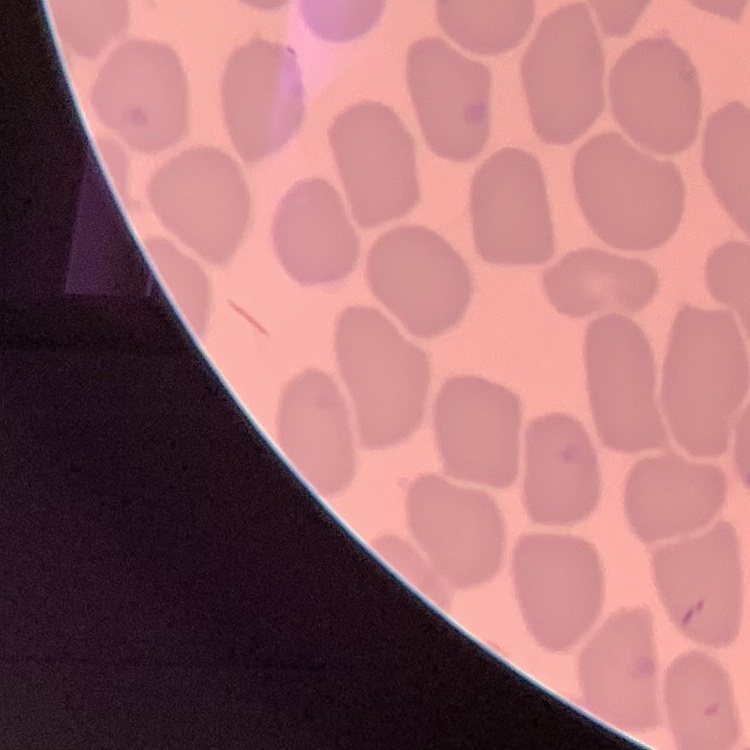

red blood cell morphology = no rouleaux formation
image type = one tile cut from a larger photomicrograph
preparation = thin blood film
stain = Field's or Giemsa